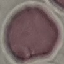

Result: no malaria parasites detected. Acquired by smartphone through the microscope eyepiece. Thin blood smear. Giemsa-stained preparation. Automatically extracted cell patch, resized to 64 × 64 pixels.